Comment on the morphology of the red blood cells.
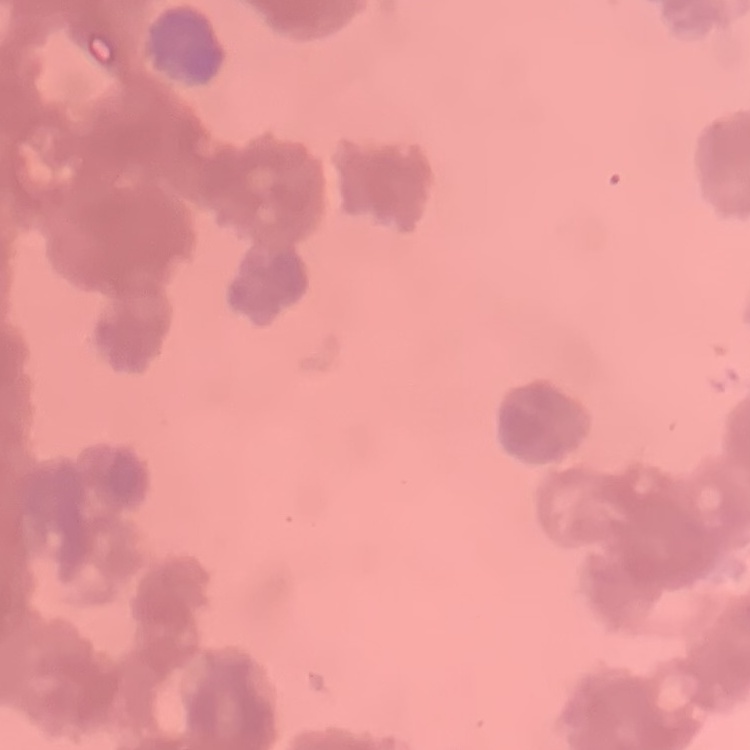

Rouleaux formation.

One tile cut from a larger photomicrograph. Stained with either Field's or Giemsa. Thin blood film.